Name the parasite shown.
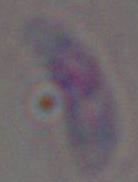

This is Toxoplasma gondii.

Summary:
  - Modality: photomicrograph
  - Magnification: 1000x